Identify the blood parasite species.
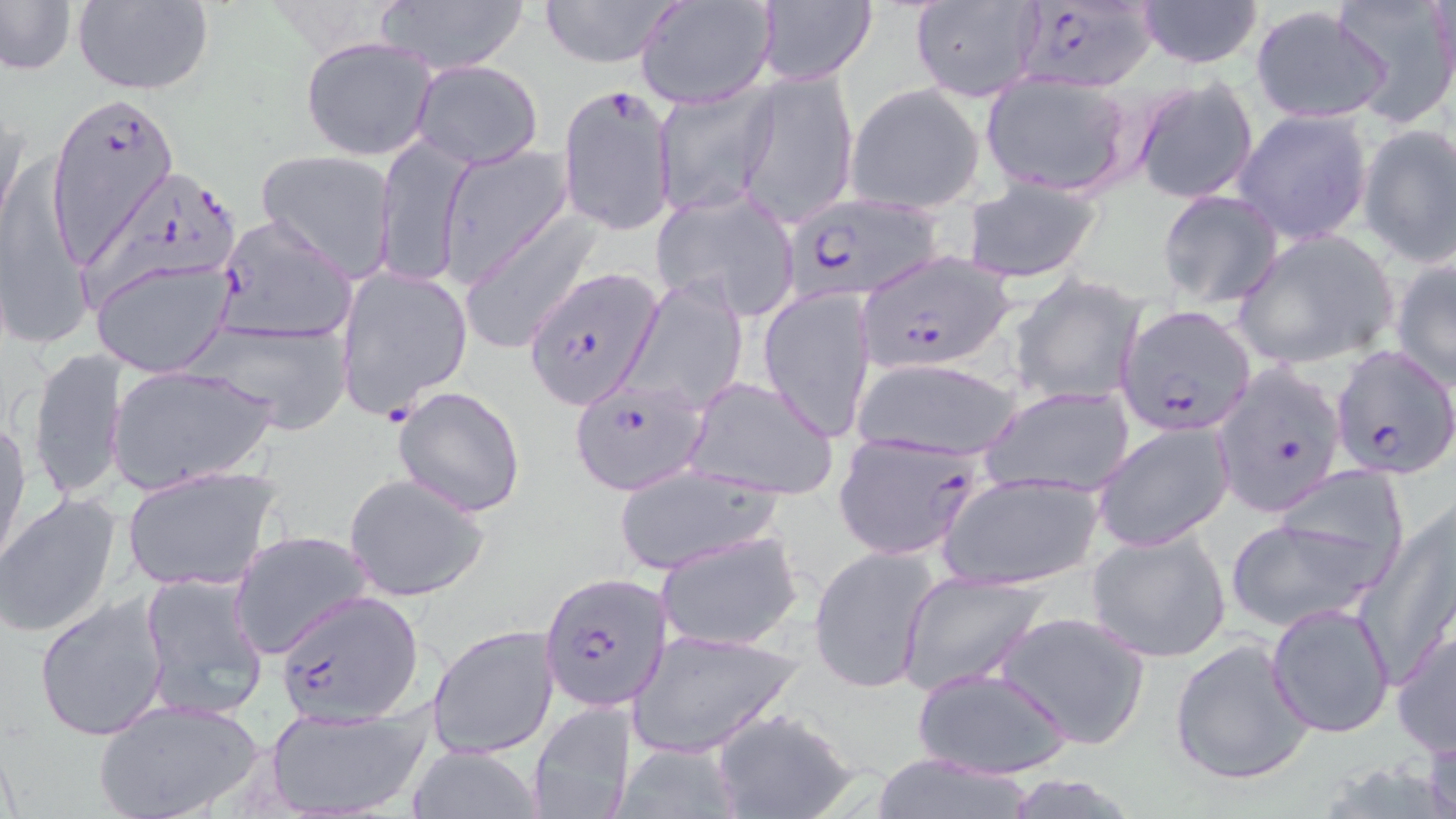

Plasmodium falciparum.

Approximate bounding boxes as (x1,y1)-(x2,y2) corner pairs in pixels. Uninfected red blood cell locations: (0,0)-(78,77), (536,0)-(683,68), (636,0)-(776,109), (1133,0)-(1265,68), (1332,0)-(1456,127), (71,1)-(214,95), (908,1)-(1043,102), (374,2)-(527,75), (754,2)-(878,86), (1250,6)-(1390,125), (301,36)-(438,161), (411,59)-(543,168), (736,68)-(858,230), (981,71)-(1134,198), (1131,77)-(1259,205), (846,84)-(985,212), (652,85)-(775,217), (0,98)-(27,242), (1232,109)-(1374,246), (1357,124)-(1456,269), (373,134)-(472,289), (437,146)-(573,285), (257,150)-(399,280), (4,154)-(86,344), (962,179)-(1102,284), (651,188)-(801,318), (1158,190)-(1283,309), (461,213)-(602,354), (1233,230)-(1400,369), (91,257)-(235,378), (1389,258)-(1456,389), (1011,274)-(1146,407), (620,276)-(750,415), (759,287)-(876,441), (194,317)-(355,431), (29,346)-(128,504), (852,355)-(1022,464), (108,364)-(273,493), (682,374)-(841,502), (982,384)-(1136,498), (388,385)-(523,515), (0,415)-(29,569), (1091,422)-(1235,553), (120,465)-(280,593), (610,466)-(783,574), (940,472)-(1104,591), (1261,472)-(1413,593), (344,473)-(491,602), (0,492)-(123,640), (1360,498)-(1456,684), (1224,515)-(1391,631), (1086,528)-(1231,664), (654,529)-(805,653), (228,530)-(374,658), (808,544)-(943,695), (898,569)-(1050,696), (137,571)-(271,721), (32,595)-(170,742), (1267,602)-(1395,738), (994,610)-(1151,750), (428,624)-(561,758), (627,627)-(804,758), (1391,627)-(1456,756), (1169,635)-(1315,788), (912,666)-(1072,780), (93,697)-(267,819), (528,701)-(640,819), (265,704)-(429,817), (710,706)-(860,819), (1422,729)-(1456,819), (614,741)-(742,819), (407,744)-(543,818), (866,752)-(1039,818). Plasmodium falciparum-infected red blood cell locations: (1007,4)-(1155,91), (556,84)-(676,238), (46,93)-(183,263), (83,170)-(237,310), (782,194)-(943,305), (213,215)-(357,348), (855,251)-(1016,372), (522,266)-(662,410), (340,269)-(477,422), (1117,306)-(1256,436), (1329,344)-(1455,477), (1214,361)-(1348,518), (568,376)-(709,495), (832,431)-(985,560), (539,573)-(670,711), (277,589)-(423,725). Captured at 1000x magnification. Optical microscopy. Thin blood smear. Single field of view. May-Grünwald-Giemsa stain. Image is 1456×819 pixels.